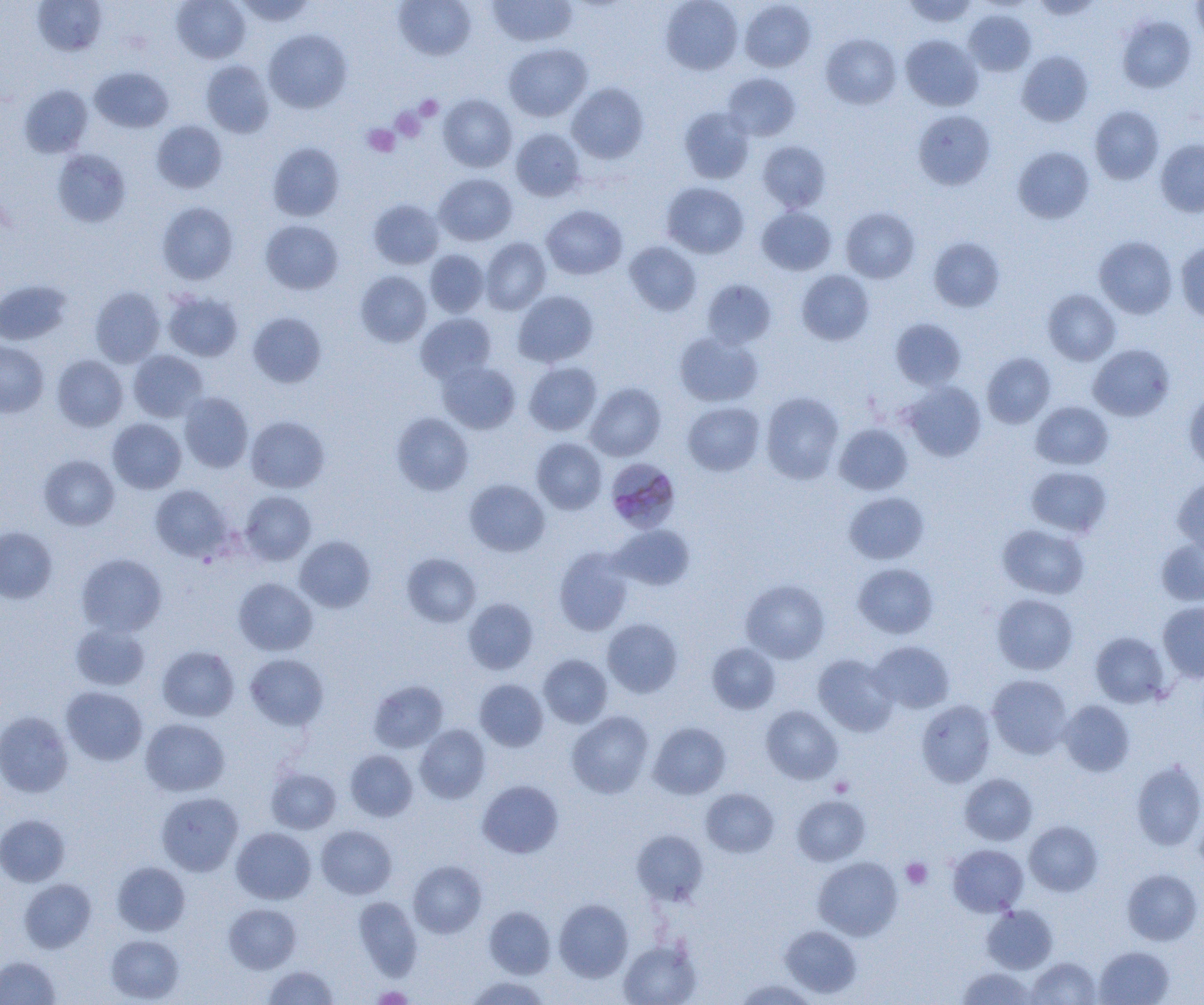

slide_level_diagnosis: Plasmodium malariae
preparation: thin blood smear
platelet_locations: 'approximate bounding boxes as [x1, y1, x2, y2] in pixels: [415, 95, 443, 121], [391, 108, 426, 142], [363, 124, 400, 157], [830, 776, 854, 797], [901, 858, 932, 889], [371, 986, 413, 1004]'
plasmodium_malariae_infected_red_blood_cell_locations: 'approximate bounding boxes as [x1, y1, x2, y2] in pixels: [606, 462, 682, 532]'
field_of_view: one of a larger specimen
uninfected_red_blood_cell_locations: 'approximate bounding boxes as [x1, y1, x2, y2] in pixels: [33, 0, 107, 56], [172, 0, 250, 63], [236, 0, 315, 26], [393, 0, 476, 61], [487, 0, 577, 47], [660, 0, 743, 75], [903, 0, 978, 27], [1031, 0, 1101, 20], [1191, 0, 1204, 43], [739, 1, 816, 72], [964, 9, 1036, 76], [1116, 15, 1196, 93], [264, 29, 352, 113], [821, 34, 901, 109], [901, 34, 983, 111], [504, 44, 592, 121], [1018, 51, 1092, 126], [201, 60, 275, 138], [90, 67, 173, 133], [722, 73, 801, 141], [566, 82, 649, 163], [19, 84, 93, 157], [438, 94, 517, 172], [1090, 106, 1164, 184], [679, 107, 754, 183], [913, 110, 995, 190], [152, 120, 227, 193], [511, 128, 585, 201], [1155, 139, 1204, 217], [758, 140, 831, 212], [267, 142, 344, 221], [1013, 146, 1094, 223], [53, 149, 130, 227], [434, 173, 517, 246], [662, 182, 749, 258], [368, 199, 444, 269], [157, 202, 238, 284], [541, 204, 627, 279], [757, 207, 836, 275], [841, 207, 920, 283], [261, 220, 343, 294], [1094, 236, 1177, 318], [928, 237, 1004, 312], [481, 238, 551, 314], [625, 242, 701, 316], [1175, 242, 1204, 322], [424, 249, 489, 317], [797, 270, 874, 345], [355, 271, 432, 347], [0, 279, 71, 344], [701, 279, 776, 349], [90, 286, 165, 367], [1043, 289, 1120, 365], [512, 290, 599, 367], [163, 291, 243, 361], [248, 312, 327, 388], [416, 313, 496, 384], [891, 318, 967, 390], [674, 332, 763, 407], [0, 340, 49, 417], [1088, 343, 1175, 421], [128, 350, 208, 422], [982, 352, 1056, 428], [52, 355, 128, 431], [437, 361, 520, 434], [524, 362, 602, 435], [903, 381, 986, 461], [585, 382, 665, 461], [1184, 389, 1204, 472], [760, 391, 844, 484], [179, 393, 253, 472], [1031, 401, 1113, 470], [683, 402, 764, 475], [391, 412, 474, 495], [246, 416, 329, 493], [108, 418, 186, 493], [834, 423, 912, 495], [532, 437, 607, 514], [39, 454, 119, 530], [1026, 466, 1112, 538], [1173, 476, 1204, 557], [464, 479, 549, 556], [150, 484, 232, 561], [240, 490, 316, 565], [844, 491, 929, 564], [997, 524, 1089, 599], [609, 525, 695, 590], [0, 527, 57, 603], [295, 535, 375, 612], [1156, 540, 1204, 605], [554, 547, 633, 636], [402, 553, 481, 627], [76, 554, 167, 637], [853, 563, 938, 638], [234, 578, 318, 655], [741, 579, 830, 664], [992, 593, 1078, 674], [464, 598, 539, 674], [1158, 601, 1204, 683], [602, 618, 683, 698], [70, 623, 150, 690], [1090, 632, 1170, 708], [869, 640, 954, 713], [707, 642, 780, 714], [157, 646, 239, 721], [245, 653, 328, 730], [538, 654, 612, 727], [813, 654, 898, 736], [987, 674, 1073, 758], [475, 679, 548, 751], [369, 680, 448, 753], [61, 687, 148, 766], [917, 700, 995, 787], [1058, 700, 1135, 776], [761, 705, 843, 784], [0, 711, 73, 798], [567, 711, 654, 798], [140, 718, 229, 796], [649, 722, 731, 799], [415, 725, 490, 804], [345, 750, 418, 821], [1131, 759, 1204, 851], [266, 767, 341, 834], [959, 773, 1037, 845], [477, 780, 563, 858], [701, 788, 778, 857], [156, 792, 243, 876], [792, 795, 870, 866], [1194, 806, 1204, 877], [0, 814, 70, 887], [1024, 821, 1102, 896], [316, 825, 397, 899], [231, 827, 316, 904], [632, 830, 708, 905], [948, 844, 1028, 916], [813, 856, 902, 941], [408, 860, 487, 938], [112, 861, 190, 935], [1122, 868, 1203, 945], [19, 878, 96, 953], [354, 896, 422, 980], [554, 900, 633, 982], [224, 903, 301, 973], [483, 905, 556, 978], [982, 905, 1057, 974], [780, 925, 861, 998], [106, 934, 184, 1003], [619, 940, 700, 1005], [1094, 946, 1174, 1005], [0, 955, 60, 1005], [1027, 957, 1101, 1004], [263, 965, 338, 1004], [957, 967, 1037, 1005], [464, 975, 551, 1004], [734, 979, 818, 1005]'
modality: light microscopy
magnification: 1000x
image_size: 1204×1005 pixels